Report the malaria status of this cell.
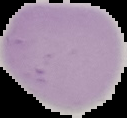

It is uninfected.

Cell region segmented out of the field of view; the surrounding area is masked to black. Image is 127×118 pixels. From a thin blood film.